Describe the morphology of the red blood cells.
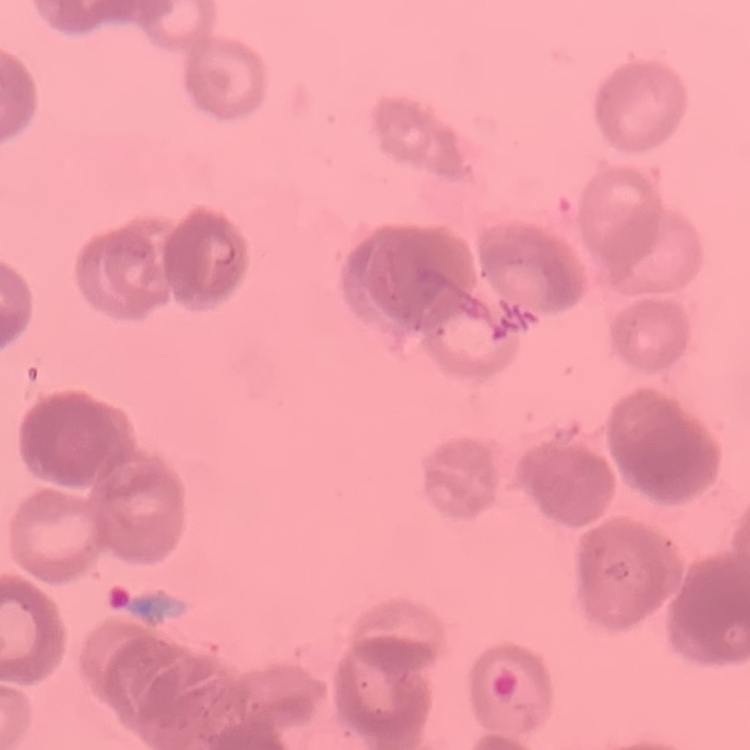

They show rouleaux formation.

Summary:
  - Image type: square crop of a larger photomicrograph
  - Preparation: thin blood smear
  - Stain: Field's or Giemsa